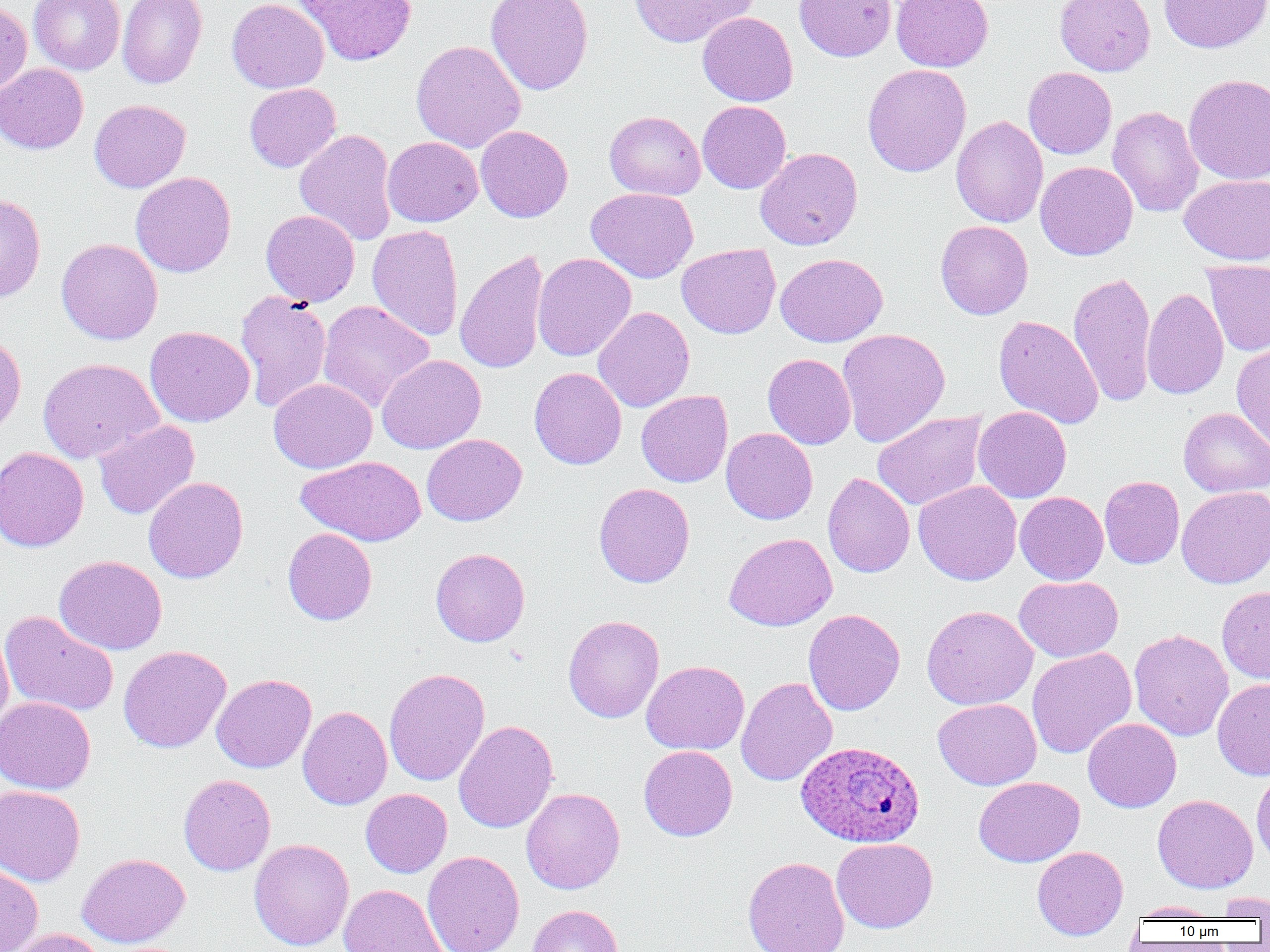

{
  "plasmodium_ovale_infected_red_blood_cell_locations": "approximate bounding boxes as [x1, y1, x2, y2] in pixels: [797, 741, 924, 848]",
  "slide_level_diagnosis": "Plasmodium ovale",
  "uninfected_red_blood_cell_locations": "approximate bounding boxes as [x1, y1, x2, y2] in pixels: [28, 0, 125, 75], [117, 0, 207, 89], [227, 0, 329, 93], [294, 0, 417, 66], [486, 0, 594, 95], [629, 0, 758, 48], [794, 0, 896, 62], [891, 0, 993, 72], [1054, 0, 1155, 76], [1158, 0, 1270, 53], [0, 1, 32, 99], [698, 11, 798, 106], [411, 39, 526, 153], [0, 63, 88, 153], [862, 64, 972, 177], [1023, 67, 1117, 159], [1183, 73, 1270, 185], [244, 83, 341, 172], [89, 99, 190, 192], [697, 100, 791, 193], [1107, 106, 1204, 218], [604, 110, 706, 200], [950, 115, 1048, 228], [475, 125, 573, 223], [294, 128, 398, 245], [383, 136, 483, 227], [755, 147, 863, 250], [1035, 161, 1138, 260], [131, 171, 236, 277], [1179, 175, 1270, 266], [586, 187, 698, 283], [0, 191, 46, 302], [260, 209, 360, 306], [935, 220, 1033, 319], [367, 224, 464, 342], [56, 238, 162, 344], [677, 243, 781, 339], [454, 249, 549, 375], [533, 252, 636, 361], [776, 253, 887, 347], [1202, 260, 1270, 357], [1067, 271, 1158, 408], [1142, 288, 1228, 399], [235, 290, 332, 413], [318, 300, 435, 413], [593, 306, 694, 412], [994, 314, 1104, 429], [145, 326, 255, 427], [837, 327, 950, 447], [0, 332, 26, 436], [1231, 341, 1270, 452], [763, 353, 856, 449], [377, 354, 486, 454], [38, 358, 162, 464], [529, 367, 627, 470], [269, 378, 377, 473], [636, 390, 732, 487], [973, 406, 1072, 503], [1179, 407, 1270, 497], [872, 411, 987, 511], [94, 420, 200, 519], [721, 428, 818, 524], [422, 434, 526, 526], [0, 447, 89, 552], [297, 456, 425, 546], [823, 472, 914, 578], [1099, 476, 1185, 568], [144, 477, 249, 583], [913, 480, 1022, 586], [593, 483, 695, 587], [1176, 486, 1270, 589], [1015, 491, 1108, 585], [283, 528, 377, 625], [724, 532, 837, 631], [430, 548, 530, 646], [54, 555, 167, 655], [1014, 575, 1123, 662], [1217, 586, 1270, 685], [922, 605, 1038, 710], [803, 609, 905, 715], [0, 610, 119, 718], [563, 615, 664, 722], [0, 627, 14, 735], [1129, 629, 1234, 741], [118, 645, 232, 752], [1027, 648, 1136, 759], [641, 661, 749, 755], [384, 668, 490, 786], [212, 674, 316, 773], [736, 676, 837, 787], [1213, 678, 1270, 780], [0, 697, 95, 794], [932, 698, 1042, 790], [298, 706, 392, 810], [1083, 718, 1182, 812], [453, 720, 558, 833], [639, 746, 737, 841], [1251, 765, 1270, 868], [178, 774, 276, 876], [974, 777, 1084, 867], [0, 785, 85, 885], [521, 788, 625, 894], [361, 789, 452, 878], [1152, 794, 1258, 893], [249, 838, 354, 951], [831, 838, 938, 933], [1032, 846, 1128, 940], [423, 851, 525, 952], [77, 852, 190, 948], [742, 856, 850, 952], [0, 864, 43, 951], [249, 868, 446, 951], [338, 884, 448, 952], [1216, 892, 1270, 919], [1129, 901, 1223, 921], [527, 905, 623, 952], [8, 928, 107, 952]",
  "preparation": "thin blood smear",
  "image_size": "1270×952 pixels",
  "magnification": "1000x",
  "field_of_view": "one of a larger specimen",
  "modality": "optical microscopy"
}